Assess this cell for malaria.
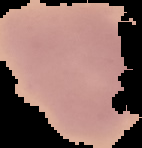
Uninfected.

{
  "image_size": "142×148 pixels",
  "preparation": "thin blood film",
  "image_type": "segmented cell region on a black background"
}